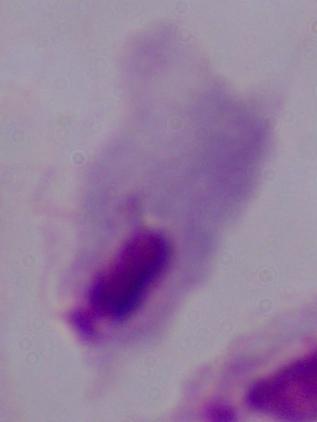
modality: photomicrograph
identification: trichomonad
magnification: 1000x